Report the malaria status of this cell.
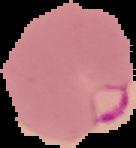
Parasitized.

image size = 136×148 pixels
preparation = thin blood film
image type = segmented cell region with the area outside set to black